Assess this cell for malaria.
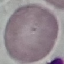
Uninfected.

Summary:
  - Stain: Giemsa
  - Preparation: thin blood film
  - Capture: smartphone through the microscope eyepiece
  - Image type: automatically extracted cell patch, resized to 64 × 64 pixels